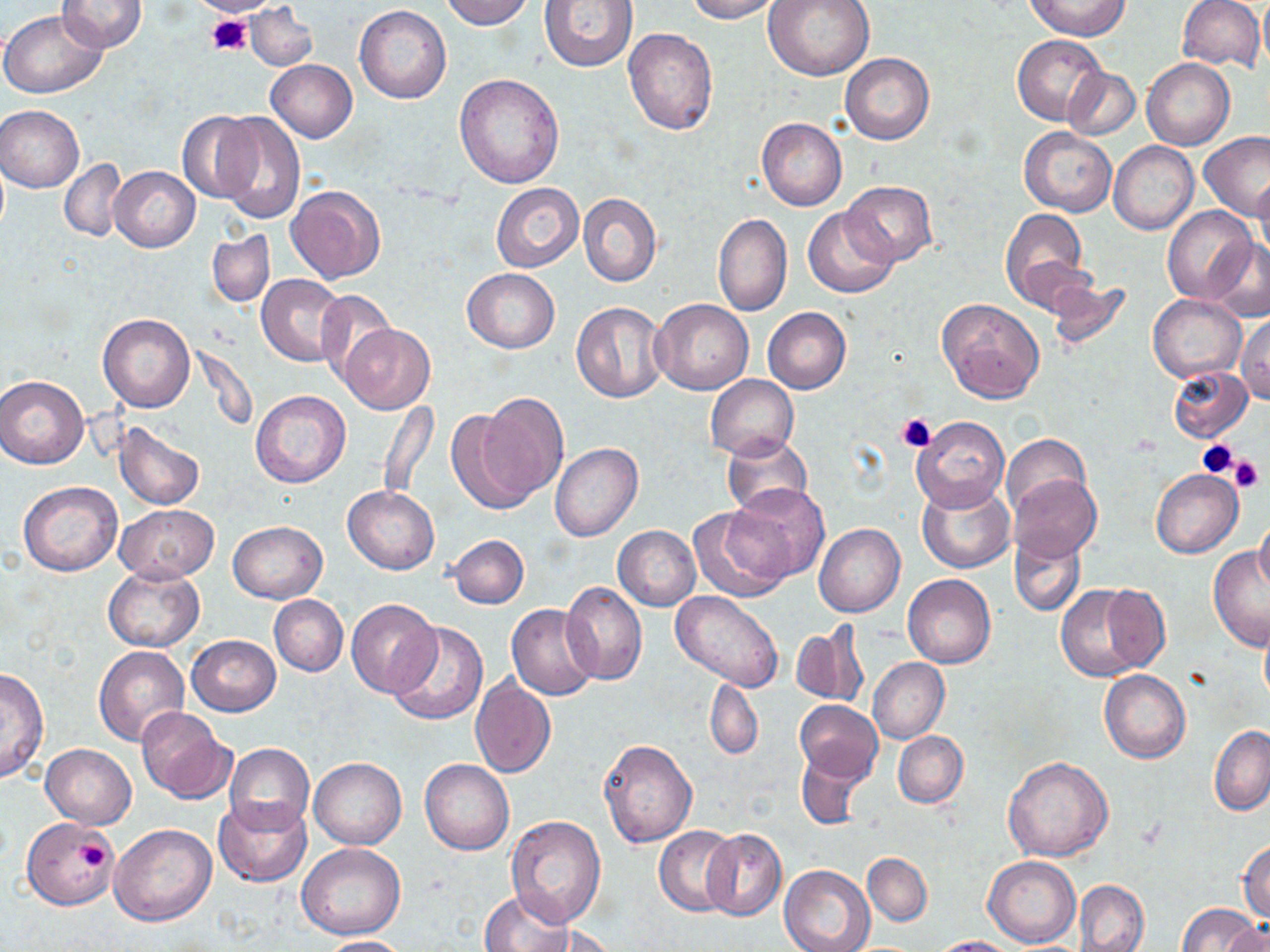

slide_level_diagnosis: no evidence of blood parasites
image_size: 1270×952 pixels
uninfected_red_blood_cell_locations: 'approximate bounding boxes as (x1,y1)-(x2,y2) corner pairs in pixels: (193,0)-(274,17), (439,0)-(534,29), (540,0)-(638,70), (685,0)-(784,22), (762,0)-(875,81), (1026,0)-(1128,39), (1176,0)-(1264,72), (1258,0)-(1270,74), (58,1)-(147,53), (245,4)-(317,71), (354,5)-(451,104), (0,9)-(107,99), (623,28)-(718,135), (1013,35)-(1107,125), (840,53)-(933,144), (1141,58)-(1234,150), (266,59)-(357,142), (1064,67)-(1140,140), (454,74)-(564,188), (1,105)-(85,192), (177,112)-(262,205), (214,112)-(305,225), (757,117)-(847,211), (1019,126)-(1116,216), (1199,133)-(1270,223), (1109,141)-(1198,234), (60,160)-(127,242), (109,167)-(200,251), (1254,171)-(1270,265), (841,181)-(938,266), (491,182)-(584,273), (286,185)-(385,284), (578,193)-(661,287), (802,207)-(898,297), (1163,207)-(1256,306), (1000,209)-(1092,306), (713,213)-(792,317), (208,231)-(274,307), (1203,238)-(1269,322), (462,269)-(559,353), (256,275)-(349,367), (1043,279)-(1133,353), (314,289)-(394,390), (1149,294)-(1246,382), (652,298)-(754,394), (937,298)-(1045,404), (572,301)-(667,402), (763,307)-(851,393), (1237,312)-(1270,404), (98,313)-(195,412), (338,322)-(435,414), (1167,366)-(1253,443), (705,374)-(798,460), (0,375)-(89,469), (251,390)-(350,487), (470,392)-(571,505), (378,401)-(438,502), (446,409)-(538,513), (910,416)-(1008,512), (114,422)-(205,510), (722,434)-(812,517), (1000,435)-(1089,516), (550,443)-(643,542), (1151,469)-(1243,558), (1008,474)-(1101,564), (18,482)-(122,576), (916,482)-(1014,573), (726,484)-(827,583), (343,486)-(438,574), (115,505)-(219,582), (688,505)-(792,602), (1253,512)-(1270,597), (228,520)-(327,603), (815,523)-(906,617), (613,525)-(701,610), (1010,531)-(1086,616), (447,534)-(529,608), (1207,548)-(1270,652), (104,565)-(204,652), (903,575)-(995,668), (560,582)-(648,686), (1055,583)-(1153,680), (1096,583)-(1173,671), (670,592)-(782,691), (270,595)-(348,677), (345,598)-(440,698), (507,604)-(600,700), (387,622)-(488,726), (791,624)-(868,708), (187,635)-(280,716), (93,647)-(189,746), (868,658)-(949,744), (0,667)-(49,785), (1099,670)-(1190,763), (471,677)-(556,778), (706,678)-(762,760), (795,700)-(882,783), (136,707)-(232,803), (1209,724)-(1270,816), (893,730)-(968,808), (599,739)-(697,847), (225,743)-(315,835), (40,744)-(137,828), (796,751)-(868,830), (309,756)-(405,849), (1003,756)-(1113,861), (420,758)-(514,856), (214,796)-(312,887), (506,815)-(605,926), (21,817)-(118,909), (110,824)-(216,927), (655,825)-(738,916), (702,828)-(786,921), (1238,840)-(1270,922), (297,843)-(406,940), (862,852)-(932,926), (983,855)-(1080,947), (778,864)-(875,952), (1074,879)-(1149,952), (480,889)-(575,952), (1177,902)-(1263,952), (1223,921)-(1270,952), (536,924)-(617,952), (314,935)-(410,951), (928,936)-(1020,952)'
field_of_view: one of a larger specimen
magnification: 1000x
stain: May-Grünwald-Giemsa
platelet_locations: 'approximate bounding boxes as (x1,y1)-(x2,y2) corner pairs in pixels: (207,14)-(253,57), (896,413)-(935,452), (1196,439)-(1239,479), (1231,455)-(1266,493), (77,842)-(108,872)'
preparation: thin blood smear
modality: optical microscopy